Point out each leukocyte.
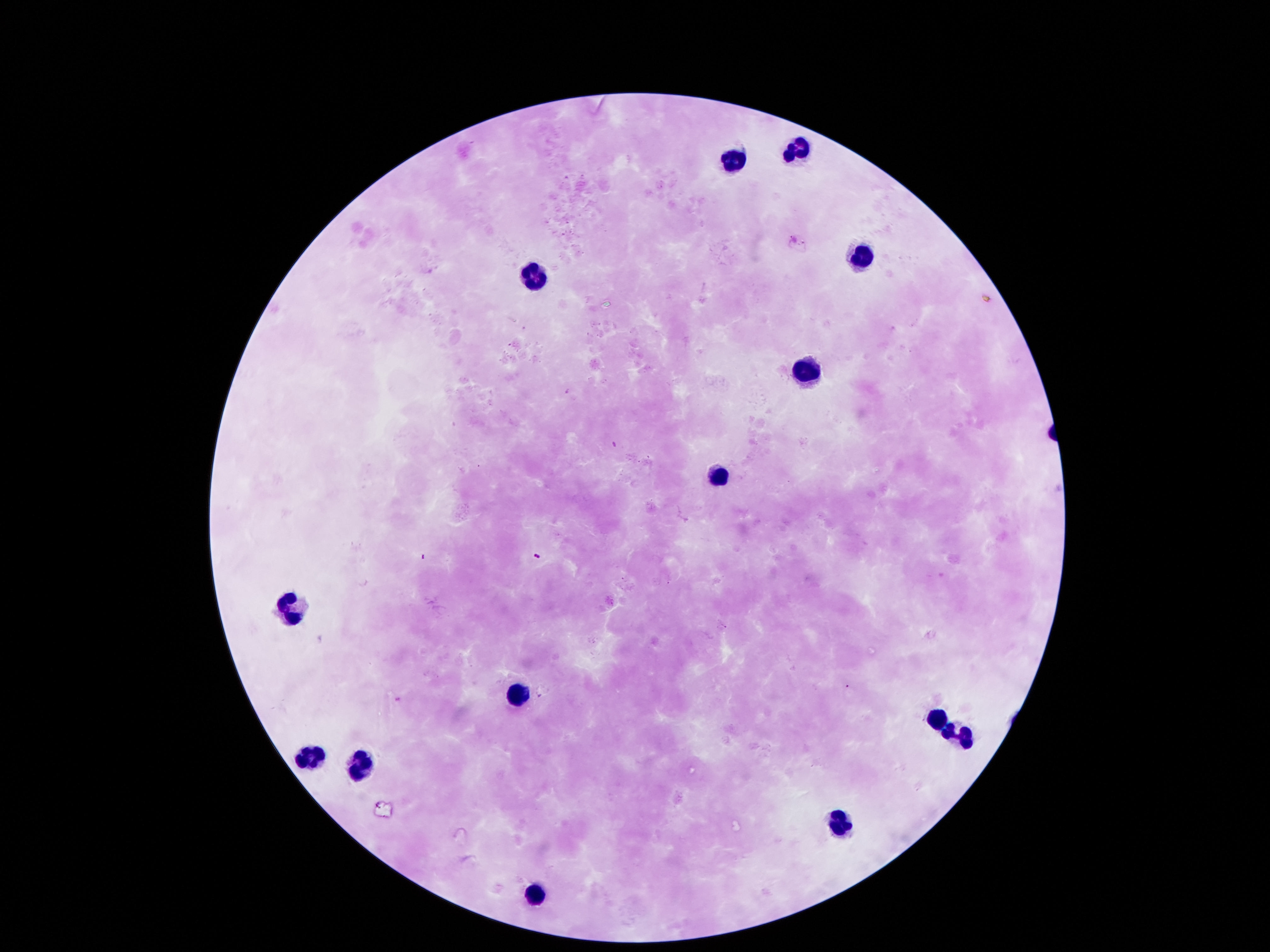

Approximate centers as {x, y} in pixels.
Leukocytes: {800, 151}, {733, 159}, {861, 253}, {538, 276}, {803, 371}, {716, 478}, {292, 605}, {518, 690}, {931, 713}, {955, 737}, {309, 757}, {356, 764}, {837, 824}, {535, 895}.

image size = 1270×952 pixels
stain = Giemsa
field of view = one from this slide
capture = smartphone camera through the microscope eyepiece
patient malaria status = uninfected
preparation = thick peripheral-blood smear
magnification = 100x